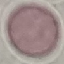

Summary:
  - Result: no malaria parasites seen
  - Image type: automatically extracted cell patch, resized to 64 × 64 pixels
  - Capture: smartphone through the microscope eyepiece
  - Stain: Giemsa
  - Preparation: thin blood film